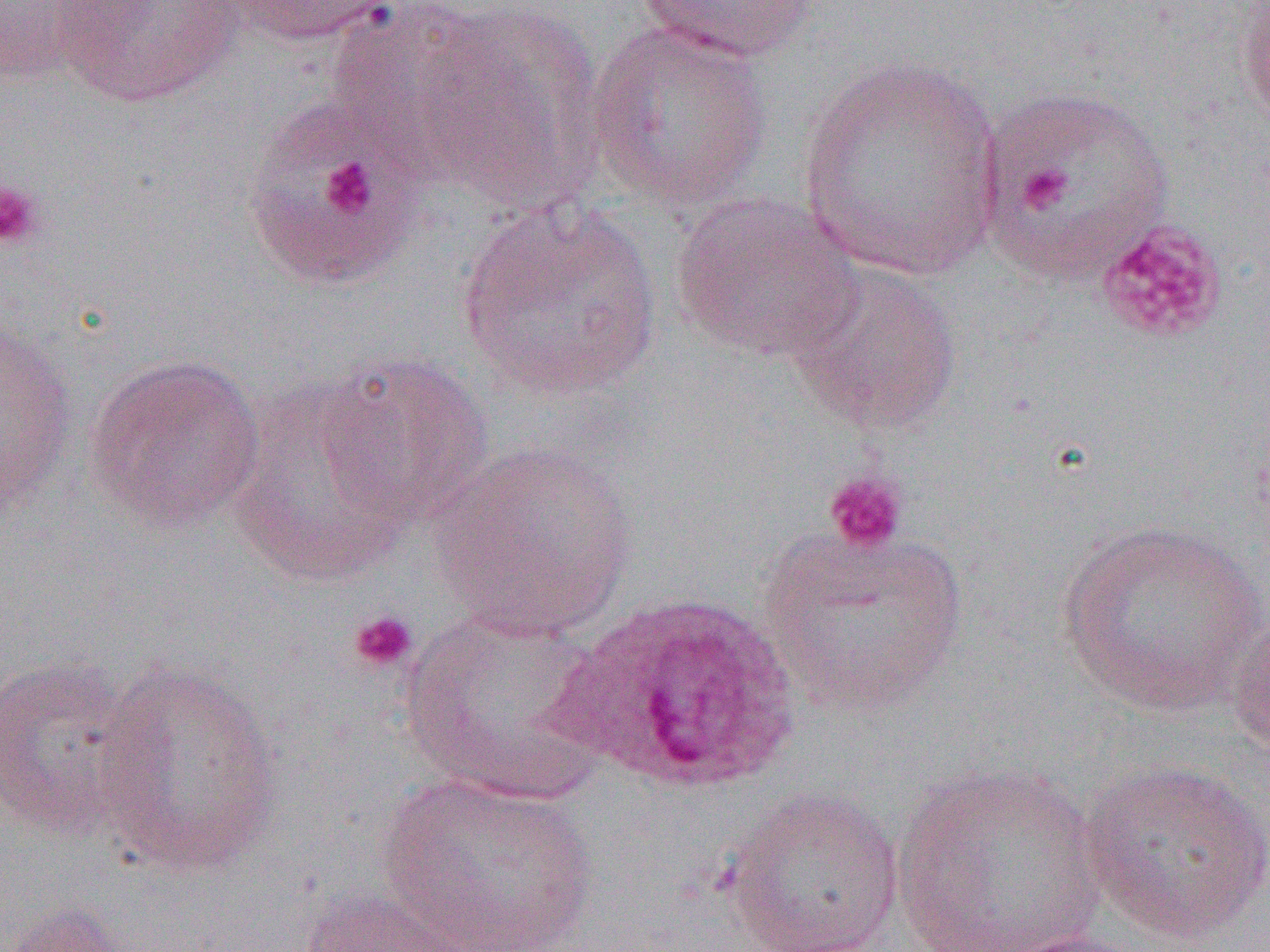 Approximate bounding boxes as [x1, y1, x2, y2] in pixels. Platelet locations: [254, 119, 419, 267], [321, 157, 376, 216], [1017, 165, 1073, 212], [0, 177, 45, 251], [1094, 219, 1229, 344], [823, 468, 910, 556], [347, 609, 418, 673]. Plasmodium ovale-infected red blood cell locations: [557, 591, 800, 795]. Uninfected red blood cell locations: [55, 0, 245, 107], [213, 0, 400, 46], [634, 0, 820, 65], [0, 1, 103, 87], [1234, 1, 1270, 132], [325, 2, 500, 164], [411, 4, 606, 208], [585, 21, 773, 212], [795, 54, 1006, 282], [975, 85, 1175, 282], [241, 102, 420, 290], [670, 192, 863, 362], [457, 197, 662, 403], [786, 260, 963, 435], [0, 322, 78, 517], [315, 351, 495, 529], [85, 352, 265, 533], [227, 376, 417, 587], [430, 440, 639, 641], [1055, 519, 1267, 718], [759, 523, 970, 718], [400, 609, 611, 802], [1226, 612, 1270, 760], [0, 654, 141, 838], [91, 659, 287, 878], [1078, 758, 1270, 945], [889, 761, 1109, 952], [375, 770, 600, 952], [720, 786, 907, 952], [297, 886, 491, 952], [2, 899, 135, 952], [996, 930, 1155, 952]. Slide-level diagnosis: Plasmodium ovale. Light microscopy. 1000x magnification. Image is 1270×952 pixels. Single field of view. Thin blood smear.